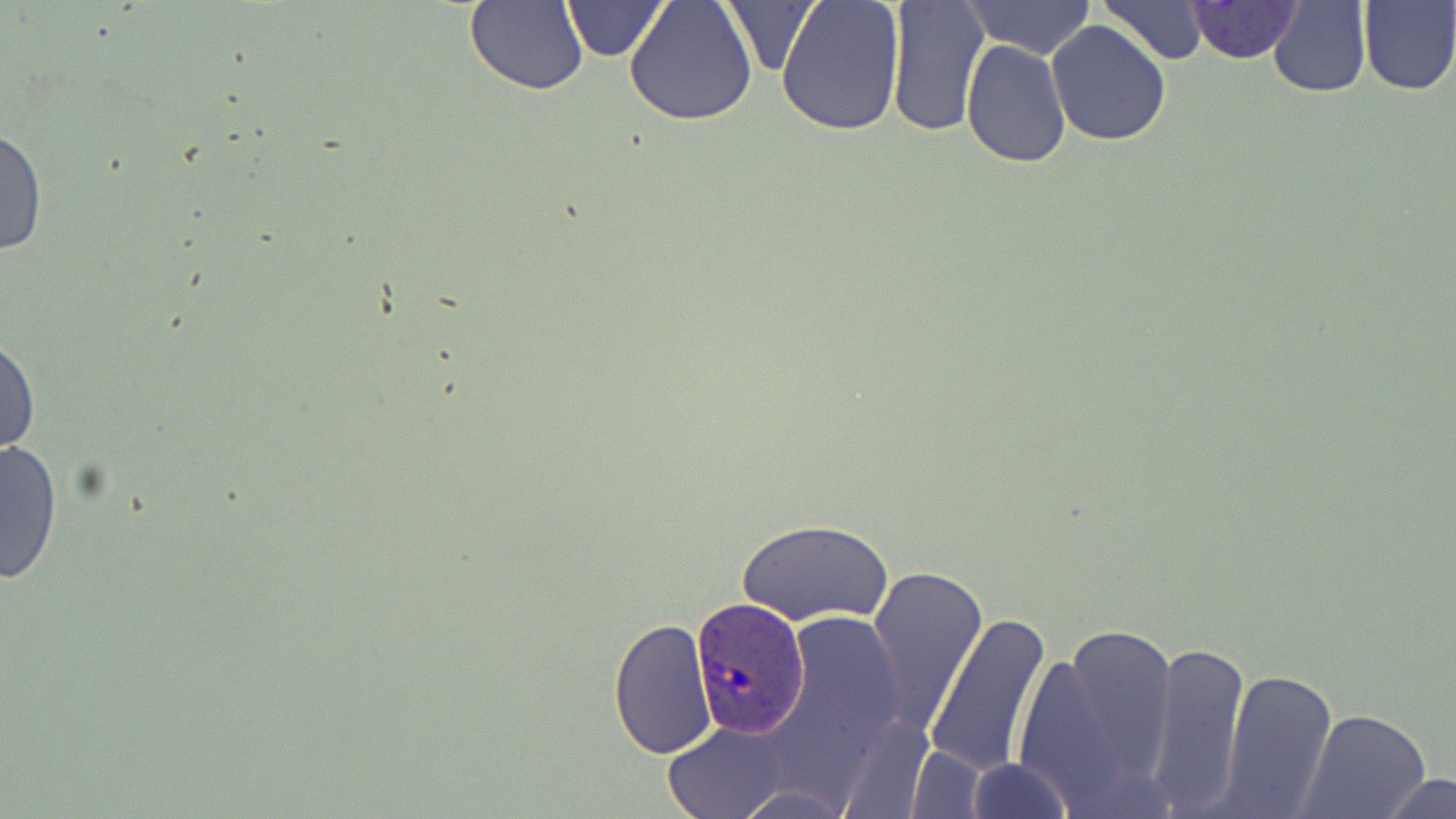
slide-level diagnosis = Plasmodium ovale
uninfected red blood cell locations = approximate bounding boxes as [x1, y1, x2, y2] in pixels: [560, 0, 671, 61], [624, 0, 758, 127], [775, 0, 907, 137], [962, 0, 1096, 62], [885, 1, 989, 137], [1099, 1, 1208, 64], [1186, 1, 1302, 64], [1268, 1, 1372, 98], [1357, 1, 1455, 94], [463, 2, 586, 95], [718, 2, 820, 78], [1046, 20, 1170, 146], [959, 38, 1071, 169], [1, 123, 47, 260], [0, 330, 40, 464], [0, 438, 63, 585], [736, 519, 892, 626], [866, 562, 987, 738], [783, 609, 907, 748], [925, 610, 1054, 778], [608, 618, 719, 759], [1022, 620, 1186, 810], [1145, 640, 1250, 812], [1219, 669, 1338, 816], [1300, 710, 1431, 819], [661, 721, 795, 819], [904, 745, 990, 817], [966, 757, 1072, 819], [1378, 772, 1455, 818], [731, 781, 853, 818]
magnification = 1000x
field of view = one of a larger specimen
Plasmodium ovale-infected red blood cell locations = approximate bounding boxes as [x1, y1, x2, y2] in pixels: [689, 598, 811, 738]
preparation = thin blood film
stain = May-Grünwald-Giemsa
image size = 1456×819 pixels
modality = optical microscopy